Point out each leukocyte.
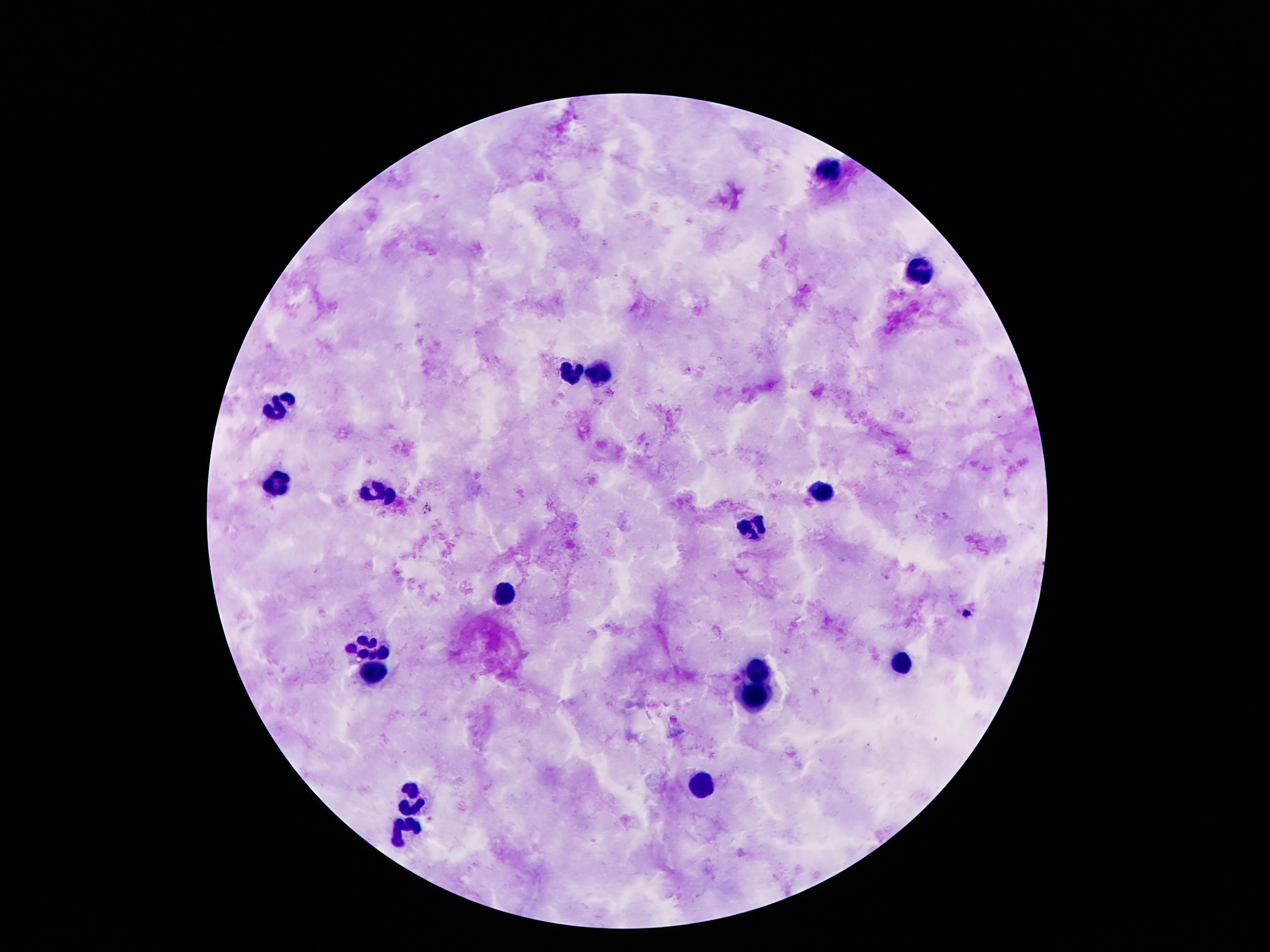
Approximate centers as (x, y) in pixels.
Leukocytes: (827, 169), (922, 271), (599, 372), (571, 374), (284, 405), (279, 481), (823, 491), (376, 492), (752, 531), (505, 594), (370, 646), (904, 660), (761, 667), (374, 669), (756, 696), (701, 784), (414, 797), (405, 830).

field_of_view: one from this slide
capture: smartphone camera through the microscope eyepiece
stain: Giemsa
patient_malaria_status: uninfected
preparation: thick blood film
image_size: 1270×952 pixels
magnification: 100x